Comment on the morphology of the red blood cells.
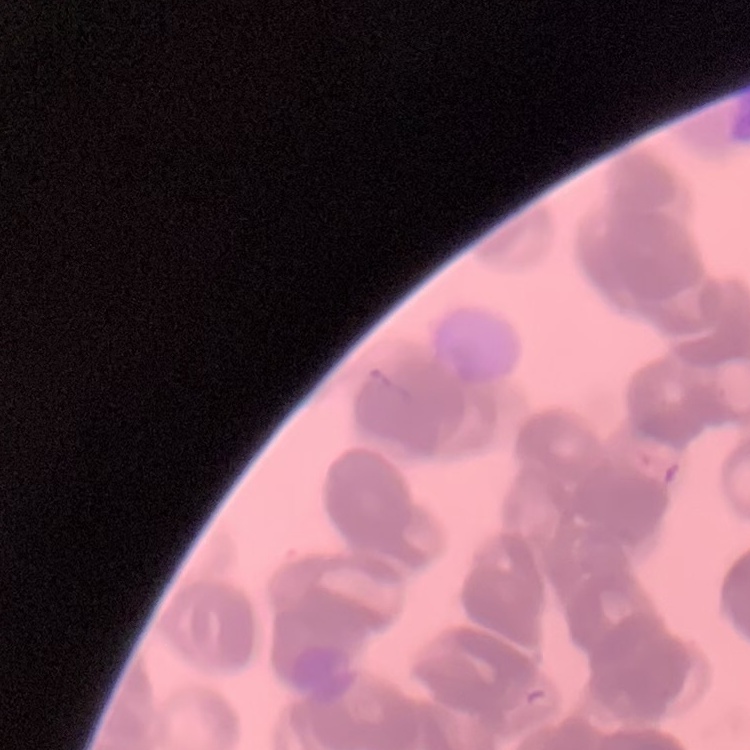

Rouleaux formation.

stain = Field's or Giemsa
preparation = thin blood film
image type = one tile cut from a larger photomicrograph